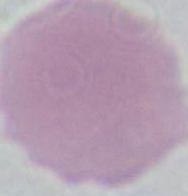

Summary:
  - Identification: erythrocyte
  - Magnification: 1000x
  - Modality: photomicrograph